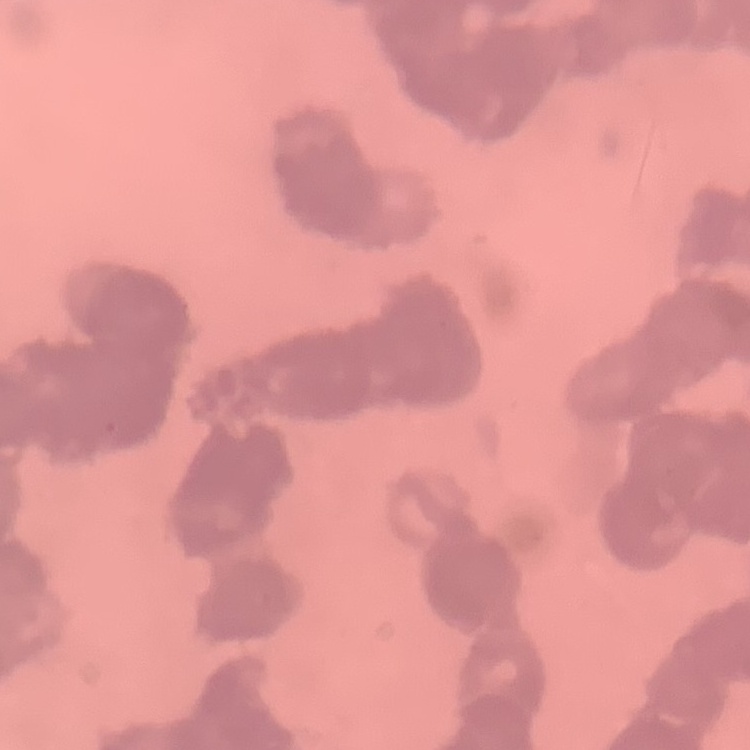

{
  "erythrocyte_morphology": "rouleaux formation",
  "preparation": "thin peripheral smear",
  "stain": "Field's or Giemsa",
  "image_type": "square crop of a larger photomicrograph"
}